Locate every blood parasite and identify its species.
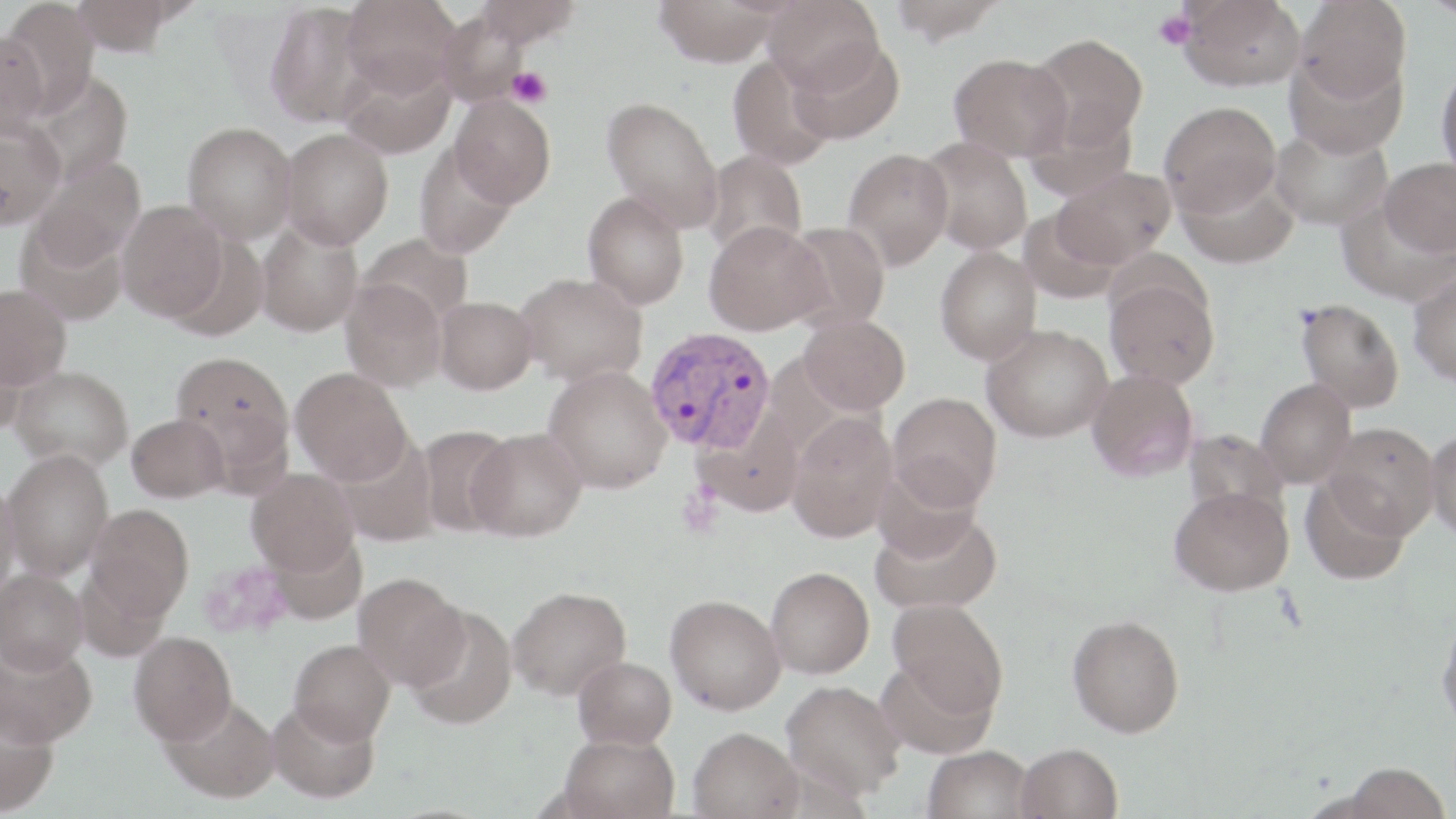
Approximate bounding boxes as (x1,y1)-(x2,y2) corner pairs in pixels.
Plasmodium vivax-infected red blood cells: (645,326)-(777,453).
No Plasmodium falciparum, Plasmodium ovale, Plasmodium malariae, Babesia divergens, or Trypanosoma brucei observed.

Platelet locations: (1153,10)-(1197,50), (508,68)-(551,108). Uninfected red blood cell locations: (1,0)-(99,116), (71,0)-(181,55), (340,0)-(461,98), (475,0)-(581,48), (653,0)-(783,66), (763,0)-(884,95), (889,0)-(1006,44), (1179,0)-(1306,91), (1295,0)-(1411,101), (264,3)-(376,128), (437,8)-(529,106), (0,27)-(50,138), (1027,34)-(1149,151), (788,39)-(905,143), (1285,50)-(1407,158), (949,53)-(1072,162), (728,54)-(836,169), (339,57)-(455,160), (1435,61)-(1456,181), (28,70)-(134,185), (449,94)-(555,208), (601,96)-(724,230), (1159,101)-(1282,216), (1025,105)-(1138,202), (0,118)-(67,229), (183,122)-(297,243), (1270,125)-(1393,230), (280,128)-(393,249), (919,138)-(1034,255), (414,141)-(519,258), (843,147)-(954,271), (702,150)-(808,260), (29,155)-(146,271), (1379,157)-(1456,257), (1176,166)-(1300,270), (1054,167)-(1175,267), (583,190)-(690,310), (1337,198)-(1454,306), (117,200)-(227,321), (1018,206)-(1122,305), (13,217)-(127,325), (704,220)-(827,336), (255,221)-(363,336), (784,221)-(890,332), (358,233)-(473,328), (935,247)-(1042,364), (1408,270)-(1456,387), (515,272)-(647,386), (1104,277)-(1220,389), (340,279)-(447,391), (0,283)-(71,388), (434,296)-(538,394), (1296,298)-(1405,413), (799,314)-(910,414), (982,324)-(1113,442), (0,338)-(28,435), (171,351)-(294,468), (9,365)-(133,471), (544,365)-(672,494), (290,367)-(412,485), (1087,369)-(1198,482), (1255,379)-(1356,487), (888,392)-(1002,510), (786,412)-(899,542), (126,413)-(229,503), (1323,422)-(1440,538), (416,424)-(517,537), (1425,426)-(1456,542), (467,427)-(587,541), (1183,428)-(1288,522), (2,448)-(113,581), (873,461)-(983,563), (247,469)-(360,576), (1300,476)-(1412,585), (0,477)-(22,601), (1169,485)-(1294,596), (86,504)-(194,618), (871,508)-(1003,615), (766,566)-(874,679), (0,567)-(88,674), (354,573)-(469,689), (507,586)-(632,700), (665,594)-(786,714), (888,598)-(1008,717), (406,606)-(517,729), (1436,609)-(1456,736), (1067,613)-(1185,737), (129,631)-(237,745), (0,638)-(97,747), (289,639)-(395,744), (574,656)-(677,748), (876,658)-(997,760), (781,681)-(906,797), (160,695)-(280,802), (266,699)-(380,803), (0,700)-(58,815), (689,727)-(803,819), (559,732)-(679,819), (1015,742)-(1123,819), (924,745)-(1034,819), (1334,762)-(1452,819). Slide-level diagnosis: Plasmodium vivax. May-Grünwald-Giemsa stain. Thin blood film. Image is 1456×819 pixels. Captured at 1000x magnification. One field of a larger specimen. Light microscopy.